Assess the morphology of the red blood cells.
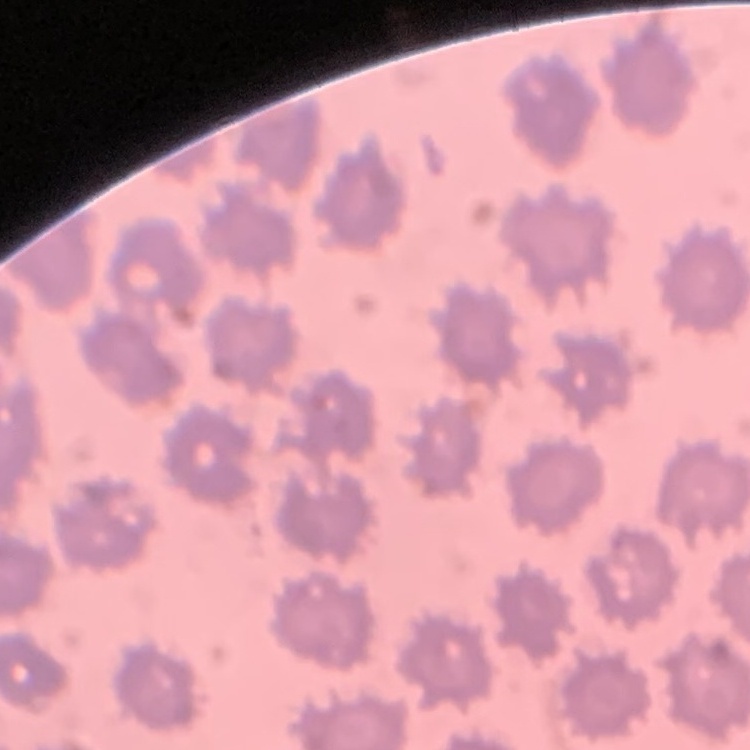

They show no rouleaux formation.

Square crop of a larger photomicrograph. Field's or Giemsa stain. Thin peripheral smear.